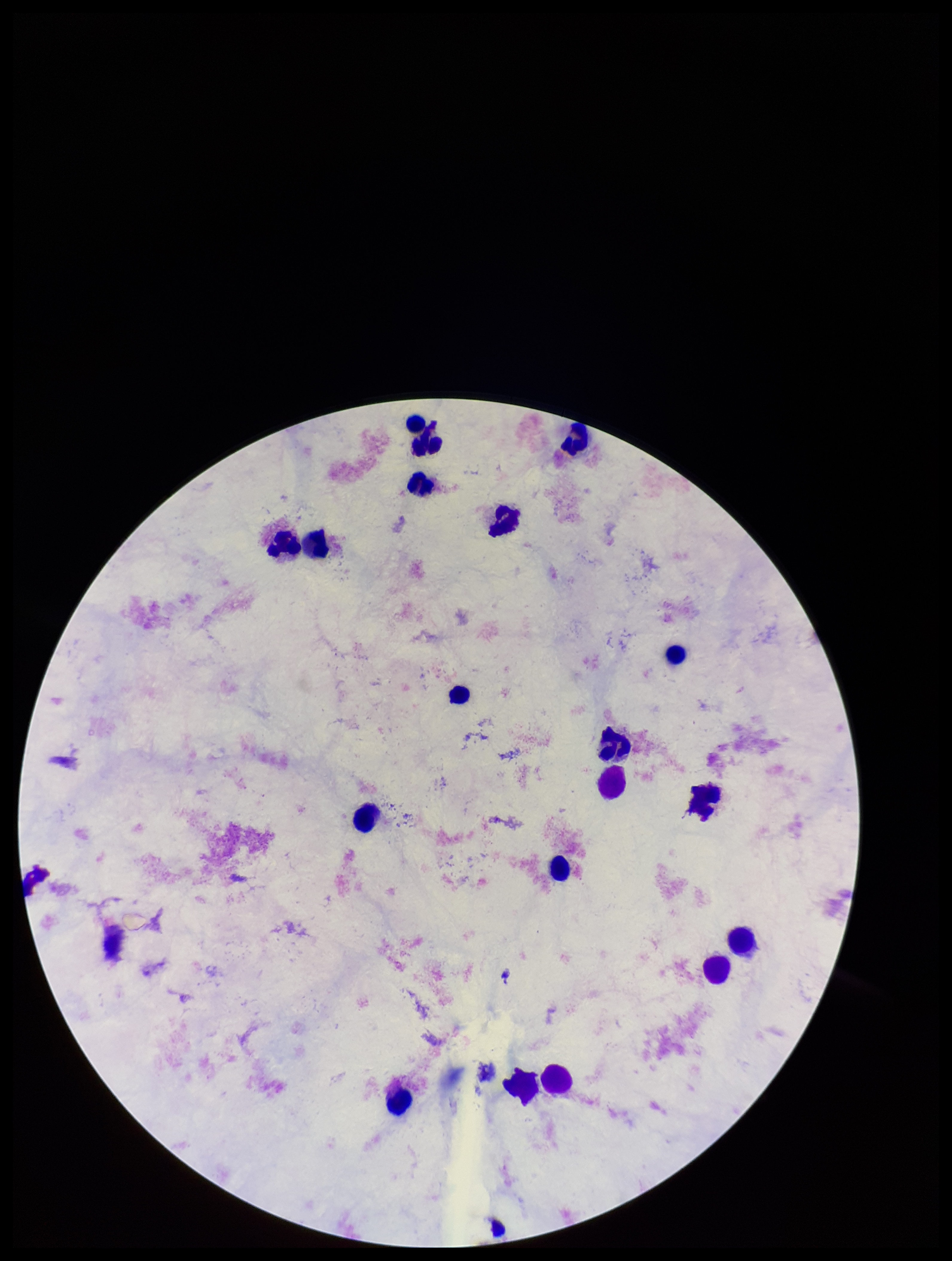
patient malaria status = negative
preparation = thick smear
parasite count = 0
Plasmodium parasites = none seen
image size = 952×1261 pixels
capture = smartphone photograph through the microscope eyepiece
leukocyte count = 18
stain = Giemsa
field of view = single